Classify this cell by malaria status.
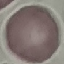
It is uninfected.

Acquired by smartphone through the microscope eyepiece. Giemsa-stained preparation. Thin smear of blood. Automatically extracted cell patch, resized to 64 × 64 pixels.